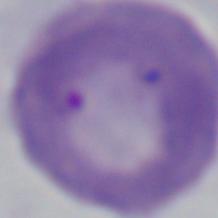

modality = photomicrograph
magnification = 1000x
identification = Babesia